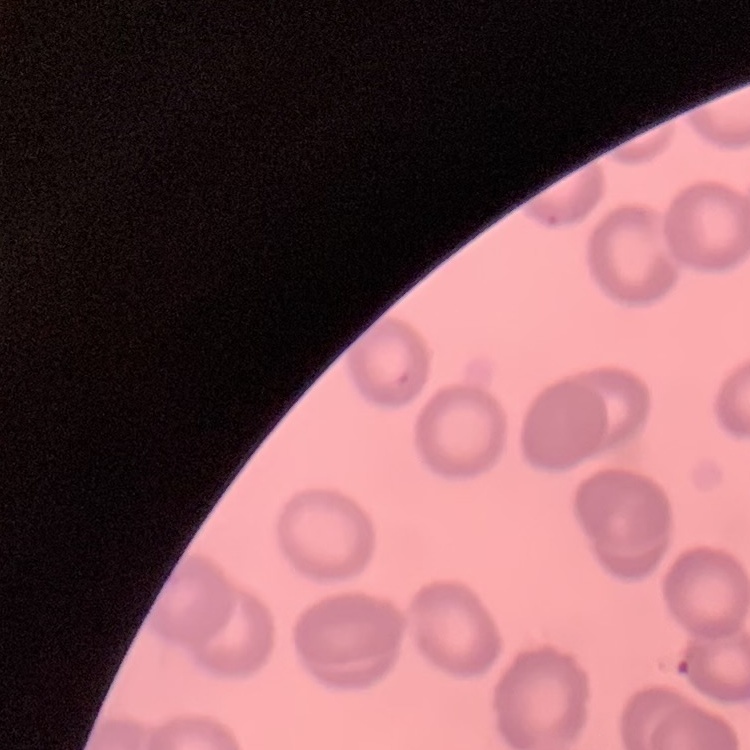
{
  "erythrocyte_morphology": "no rouleaux formation",
  "image_type": "one tile cut from a larger photomicrograph",
  "preparation": "thin blood film",
  "stain": "Field's or Giemsa"
}